Identify the preparation type.
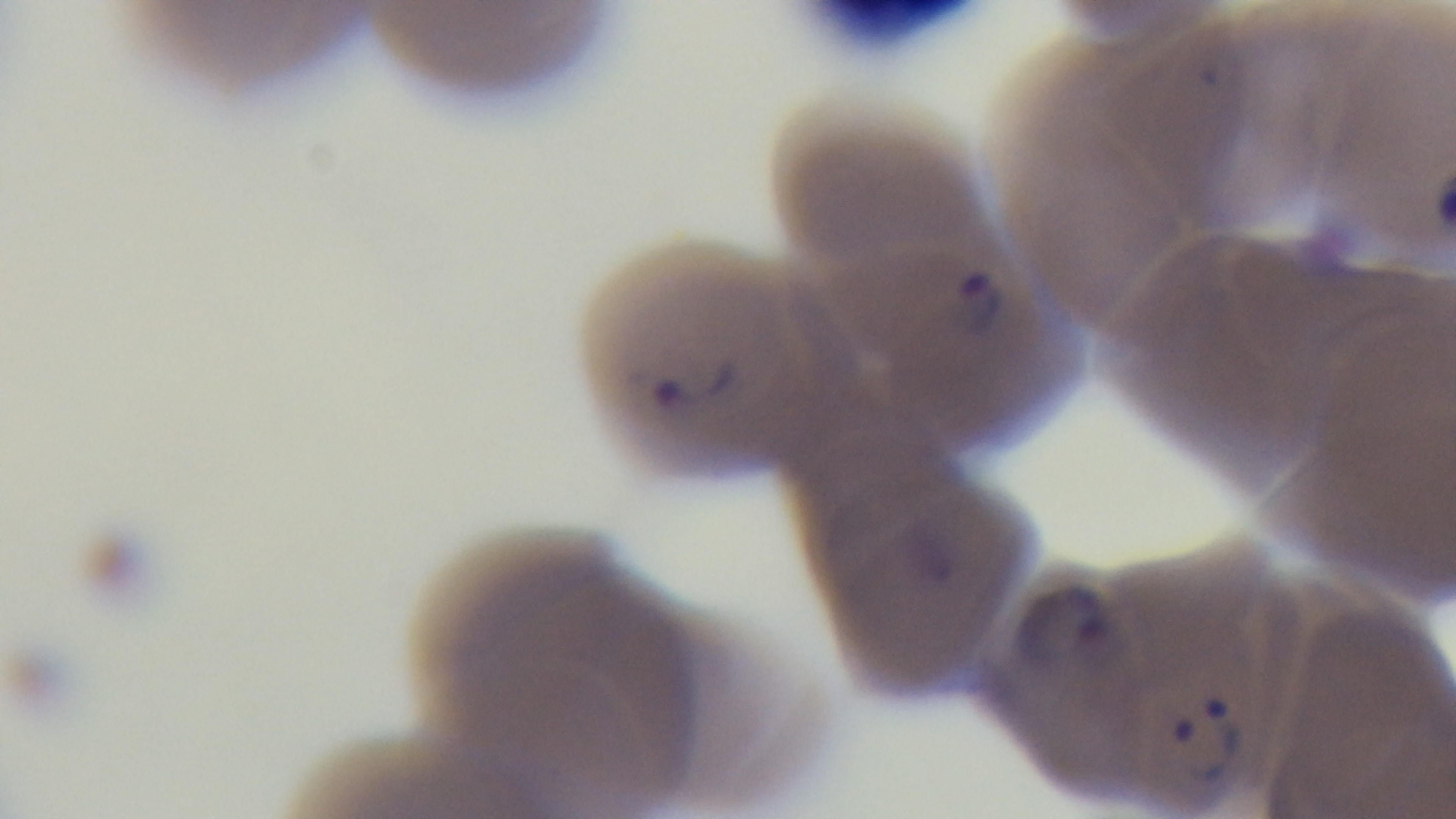

Thin.

stain: Giemsa
capture: mounted 4K digital camera
objective: 100x oil immersion
field_of_view: single
modality: light microscopy
malaria_status: infected